Locate platelets.
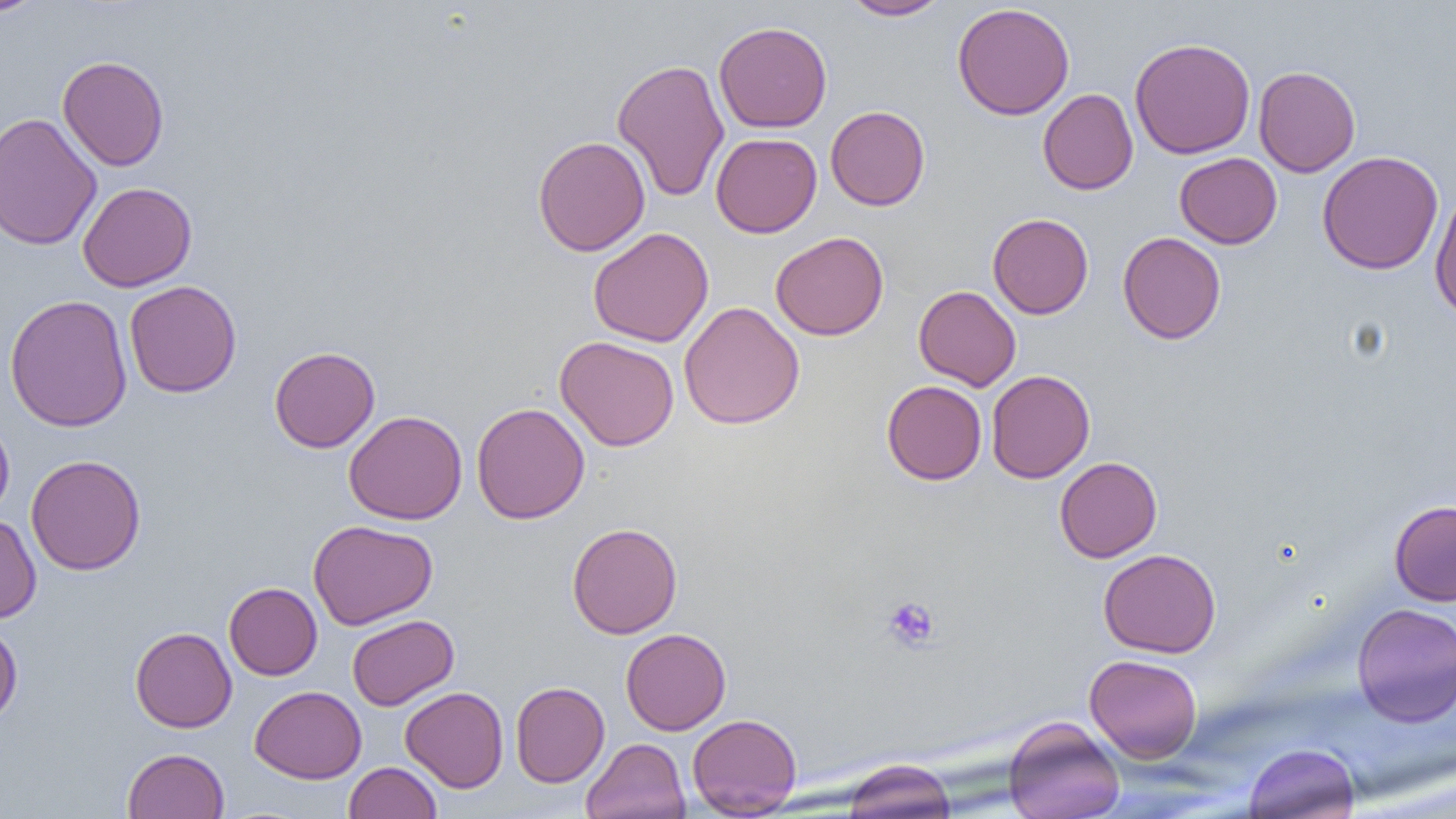
Approximate bounding boxes as named x1/y1/x2/y2 corners in pixels.
Platelets: (x1=882, y1=596, x2=940, y2=651).

slide-level diagnosis = no evidence of blood parasites
modality = light microscopy
field of view = one of a larger specimen
uninfected red blood cell locations = approximate bounding boxes as named x1/y1/x2/y2 corners in pixels: (x1=0, y1=0, x2=48, y2=18), (x1=841, y1=0, x2=953, y2=21), (x1=952, y1=3, x2=1075, y2=120), (x1=714, y1=21, x2=832, y2=133), (x1=1129, y1=37, x2=1256, y2=159), (x1=57, y1=55, x2=169, y2=171), (x1=611, y1=58, x2=729, y2=202), (x1=1253, y1=66, x2=1360, y2=177), (x1=1038, y1=88, x2=1138, y2=195), (x1=825, y1=105, x2=930, y2=210), (x1=0, y1=112, x2=102, y2=251), (x1=711, y1=132, x2=822, y2=238), (x1=533, y1=135, x2=650, y2=257), (x1=1317, y1=150, x2=1444, y2=274), (x1=1174, y1=153, x2=1282, y2=249), (x1=78, y1=182, x2=197, y2=292), (x1=1429, y1=189, x2=1456, y2=321), (x1=988, y1=213, x2=1093, y2=319), (x1=588, y1=227, x2=714, y2=347), (x1=770, y1=231, x2=889, y2=341), (x1=1117, y1=231, x2=1226, y2=344), (x1=124, y1=280, x2=242, y2=398), (x1=914, y1=285, x2=1021, y2=391), (x1=4, y1=294, x2=133, y2=432), (x1=678, y1=302, x2=805, y2=429), (x1=555, y1=336, x2=680, y2=451), (x1=268, y1=346, x2=380, y2=453), (x1=986, y1=369, x2=1095, y2=483), (x1=881, y1=380, x2=987, y2=485), (x1=471, y1=402, x2=590, y2=525), (x1=343, y1=410, x2=467, y2=525), (x1=0, y1=417, x2=15, y2=520), (x1=26, y1=454, x2=147, y2=575), (x1=1054, y1=457, x2=1162, y2=562), (x1=1388, y1=499, x2=1456, y2=606), (x1=0, y1=513, x2=41, y2=624), (x1=308, y1=519, x2=438, y2=629), (x1=566, y1=522, x2=683, y2=638), (x1=1098, y1=548, x2=1221, y2=658), (x1=224, y1=582, x2=323, y2=680), (x1=1351, y1=602, x2=1456, y2=725), (x1=346, y1=614, x2=459, y2=711), (x1=0, y1=622, x2=23, y2=725), (x1=130, y1=626, x2=237, y2=732), (x1=621, y1=628, x2=731, y2=734), (x1=1084, y1=654, x2=1203, y2=762), (x1=510, y1=681, x2=610, y2=787), (x1=250, y1=685, x2=367, y2=783), (x1=400, y1=686, x2=509, y2=792), (x1=687, y1=713, x2=802, y2=817), (x1=1003, y1=716, x2=1125, y2=819), (x1=581, y1=737, x2=690, y2=819), (x1=1242, y1=742, x2=1360, y2=819), (x1=122, y1=748, x2=229, y2=819), (x1=841, y1=759, x2=957, y2=818), (x1=344, y1=761, x2=442, y2=819)
magnification = 1000x
image size = 1456×819 pixels
preparation = thin blood film